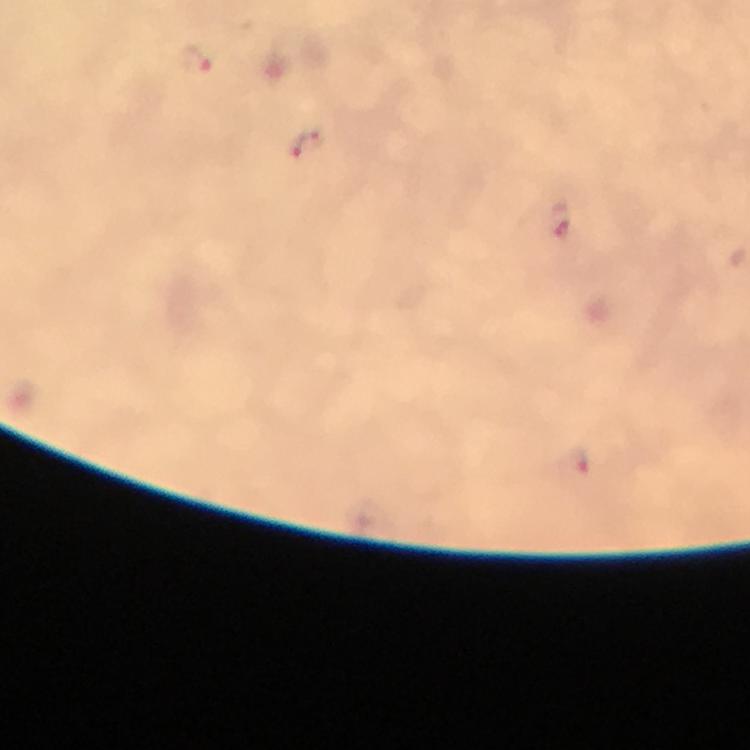
Approximate centers as [x, y] in pixels. Malaria parasite locations: [193, 59], [307, 144], [561, 219], [580, 461]. From a malaria diagnostic workup. 100x magnification. Thick blood smear. Immersion oil was used. Cropped region of a single field of view. Image is 750×750 pixels. Giemsa stain. Photographed through the microscope with a smartphone camera.